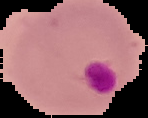

result = Plasmodium parasites identified
image type = segmented cell region on a black background
image size = 148×118 pixels
preparation = thin blood smear